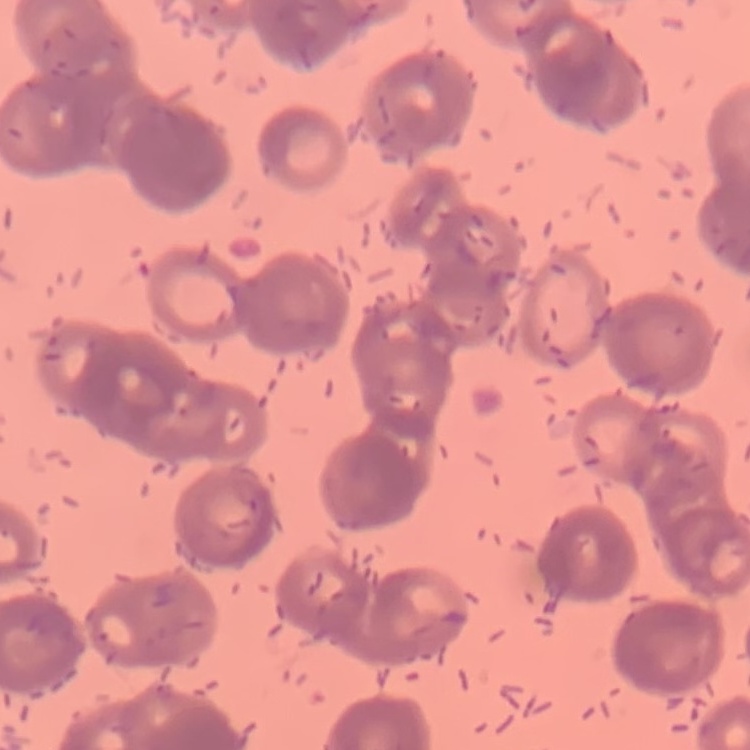

Summary:
  - Erythrocyte morphology: rouleaux formation
  - Preparation: thin blood film
  - Stain: Field's or Giemsa
  - Image type: one tile cut from a larger photomicrograph